Locate every Babesia divergens-infected red blood cell.
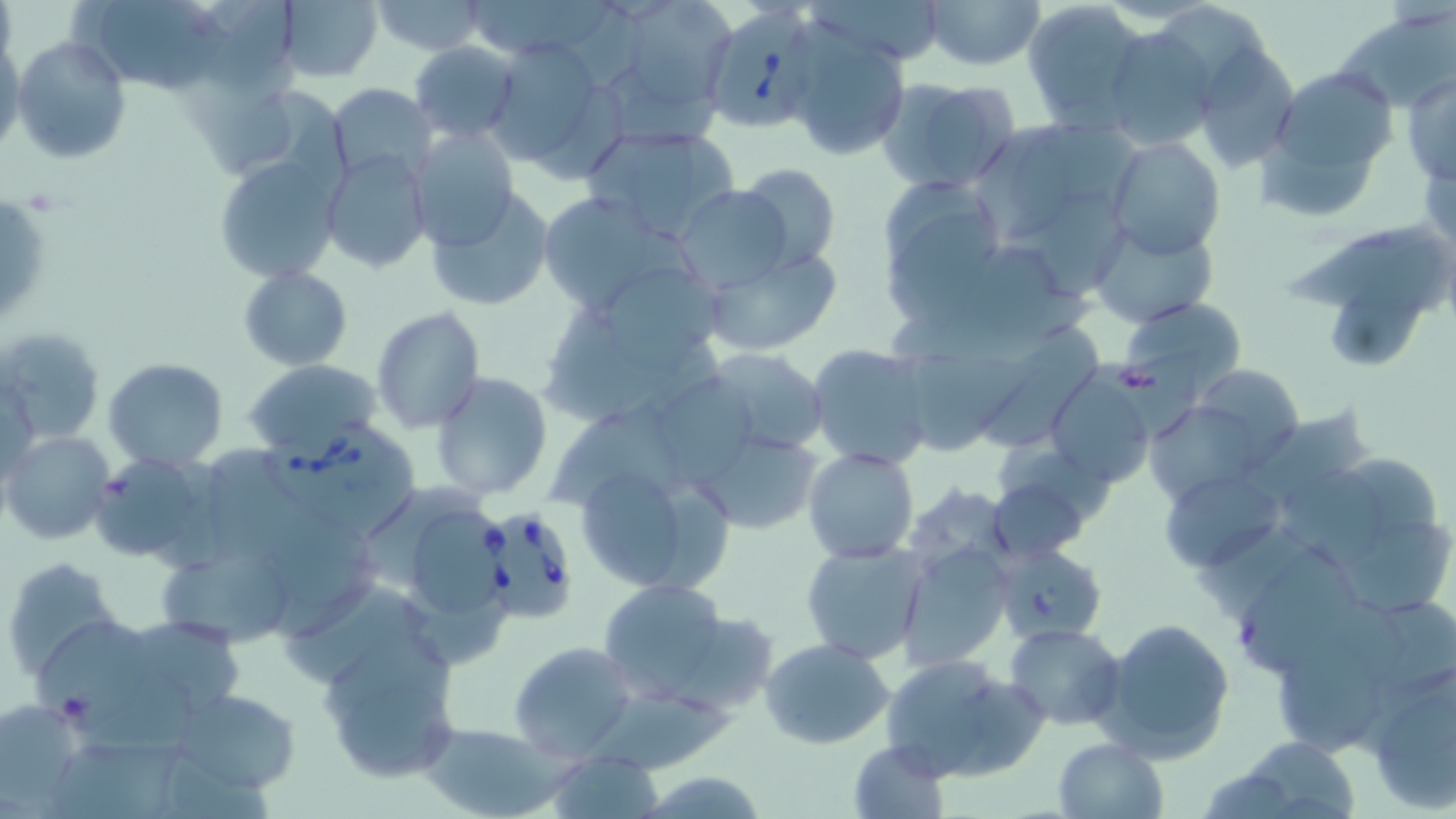
Approximate bounding boxes as named x1/y1/x2/y2 corners in pixels.
Babesia divergens-infected red blood cells: (x1=699, y1=3, x2=825, y2=133), (x1=260, y1=418, x2=423, y2=540), (x1=477, y1=504, x2=580, y2=627).

slide_level_diagnosis: Babesia divergens
stain: May-Grünwald-Giemsa
modality: light microscopy
uninfected_red_blood_cell_locations: 'approximate bounding boxes as named x1/y1/x2/y2 corners in pixels: (x1=88, y1=0, x2=225, y2=92), (x1=207, y1=0, x2=294, y2=90), (x1=278, y1=0, x2=382, y2=83), (x1=370, y1=0, x2=488, y2=55), (x1=469, y1=0, x2=615, y2=54), (x1=812, y1=0, x2=949, y2=63), (x1=922, y1=0, x2=1045, y2=71), (x1=628, y1=1, x2=736, y2=101), (x1=1021, y1=1, x2=1145, y2=132), (x1=1162, y1=2, x2=1272, y2=109), (x1=1333, y1=7, x2=1452, y2=110), (x1=1100, y1=24, x2=1216, y2=151), (x1=785, y1=28, x2=910, y2=160), (x1=482, y1=35, x2=619, y2=171), (x1=10, y1=36, x2=132, y2=164), (x1=0, y1=39, x2=24, y2=158), (x1=411, y1=43, x2=520, y2=143), (x1=1190, y1=43, x2=1300, y2=172), (x1=1257, y1=60, x2=1398, y2=218), (x1=610, y1=71, x2=717, y2=146), (x1=1402, y1=73, x2=1455, y2=185), (x1=877, y1=77, x2=1020, y2=195), (x1=327, y1=83, x2=436, y2=182), (x1=237, y1=90, x2=351, y2=211), (x1=1016, y1=119, x2=1142, y2=209), (x1=582, y1=122, x2=741, y2=241), (x1=407, y1=127, x2=519, y2=250), (x1=980, y1=130, x2=1069, y2=233), (x1=1106, y1=137, x2=1226, y2=260), (x1=320, y1=149, x2=431, y2=273), (x1=213, y1=155, x2=344, y2=282), (x1=732, y1=164, x2=842, y2=273), (x1=875, y1=173, x2=1005, y2=322), (x1=675, y1=184, x2=797, y2=291), (x1=428, y1=188, x2=555, y2=312), (x1=533, y1=189, x2=692, y2=317), (x1=1, y1=191, x2=50, y2=330), (x1=1037, y1=195, x2=1127, y2=299), (x1=1088, y1=219, x2=1216, y2=328), (x1=1285, y1=225, x2=1439, y2=307), (x1=969, y1=244, x2=1054, y2=340), (x1=1330, y1=244, x2=1437, y2=370), (x1=703, y1=247, x2=841, y2=354), (x1=238, y1=266, x2=350, y2=370), (x1=538, y1=270, x2=728, y2=433), (x1=1119, y1=297, x2=1246, y2=393), (x1=372, y1=307, x2=486, y2=432), (x1=982, y1=323, x2=1107, y2=447), (x1=3, y1=325, x2=106, y2=445), (x1=806, y1=344, x2=934, y2=471), (x1=698, y1=346, x2=831, y2=456), (x1=103, y1=357, x2=228, y2=470), (x1=902, y1=357, x2=1035, y2=457), (x1=245, y1=359, x2=382, y2=462), (x1=1192, y1=365, x2=1305, y2=464), (x1=431, y1=371, x2=555, y2=500), (x1=1045, y1=373, x2=1155, y2=489), (x1=1144, y1=400, x2=1270, y2=508), (x1=1255, y1=409, x2=1369, y2=498), (x1=692, y1=430, x2=821, y2=534), (x1=4, y1=432, x2=114, y2=545), (x1=204, y1=444, x2=298, y2=558), (x1=803, y1=447, x2=920, y2=565), (x1=90, y1=452, x2=222, y2=565), (x1=1353, y1=456, x2=1437, y2=541), (x1=569, y1=457, x2=734, y2=597), (x1=987, y1=460, x2=1096, y2=563), (x1=1273, y1=468, x2=1387, y2=566), (x1=1162, y1=470, x2=1286, y2=573), (x1=357, y1=483, x2=484, y2=588), (x1=411, y1=506, x2=490, y2=616), (x1=270, y1=508, x2=371, y2=606), (x1=1342, y1=521, x2=1453, y2=611), (x1=801, y1=541, x2=928, y2=664), (x1=992, y1=543, x2=1109, y2=644), (x1=897, y1=545, x2=1010, y2=668), (x1=1241, y1=552, x2=1354, y2=676), (x1=4, y1=555, x2=123, y2=680), (x1=165, y1=559, x2=291, y2=645), (x1=597, y1=579, x2=731, y2=703), (x1=287, y1=582, x2=425, y2=685), (x1=405, y1=585, x2=508, y2=671), (x1=1382, y1=598, x2=1456, y2=685), (x1=678, y1=612, x2=777, y2=713), (x1=1095, y1=617, x2=1235, y2=763), (x1=32, y1=619, x2=147, y2=738), (x1=1005, y1=622, x2=1125, y2=731), (x1=139, y1=624, x2=239, y2=708), (x1=321, y1=629, x2=455, y2=727), (x1=760, y1=637, x2=895, y2=749), (x1=509, y1=641, x2=638, y2=761), (x1=1276, y1=641, x2=1381, y2=755), (x1=883, y1=656, x2=991, y2=784), (x1=1361, y1=657, x2=1456, y2=813), (x1=957, y1=677, x2=1055, y2=780), (x1=85, y1=682, x2=201, y2=761), (x1=171, y1=687, x2=301, y2=793), (x1=587, y1=688, x2=738, y2=772), (x1=340, y1=689, x2=456, y2=784), (x1=0, y1=700, x2=87, y2=810), (x1=421, y1=722, x2=558, y2=818), (x1=1238, y1=734, x2=1362, y2=818), (x1=55, y1=736, x2=185, y2=819), (x1=1053, y1=737, x2=1167, y2=819), (x1=848, y1=740, x2=950, y2=817), (x1=544, y1=753, x2=665, y2=819), (x1=1196, y1=764, x2=1305, y2=819), (x1=637, y1=768, x2=769, y2=818)'
preparation: thin blood film
magnification: 1000x
image_size: 1456×819 pixels
field_of_view: one of a larger specimen